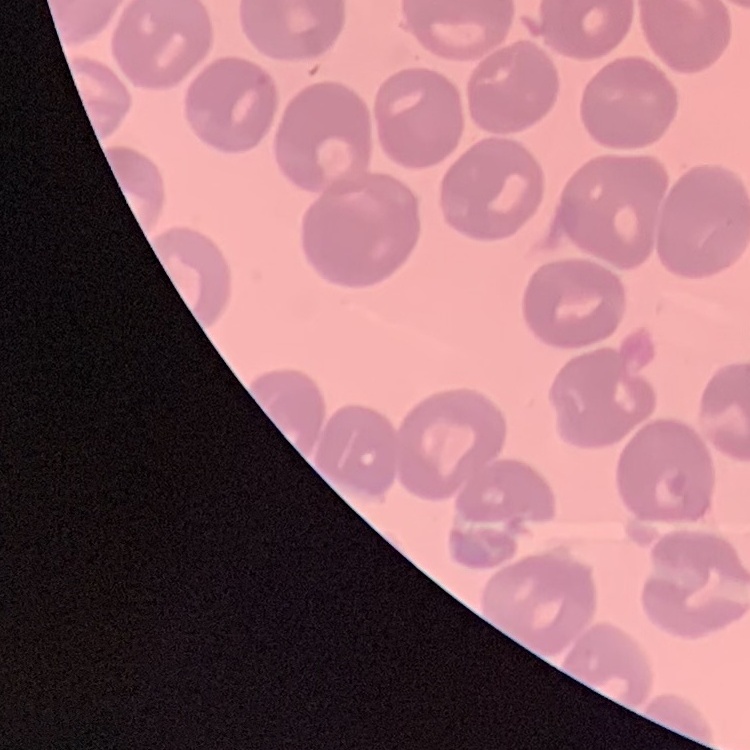
erythrocyte morphology = no rouleaux formation
stain = Field's or Giemsa
preparation = thin blood film
image type = square crop of a larger photomicrograph